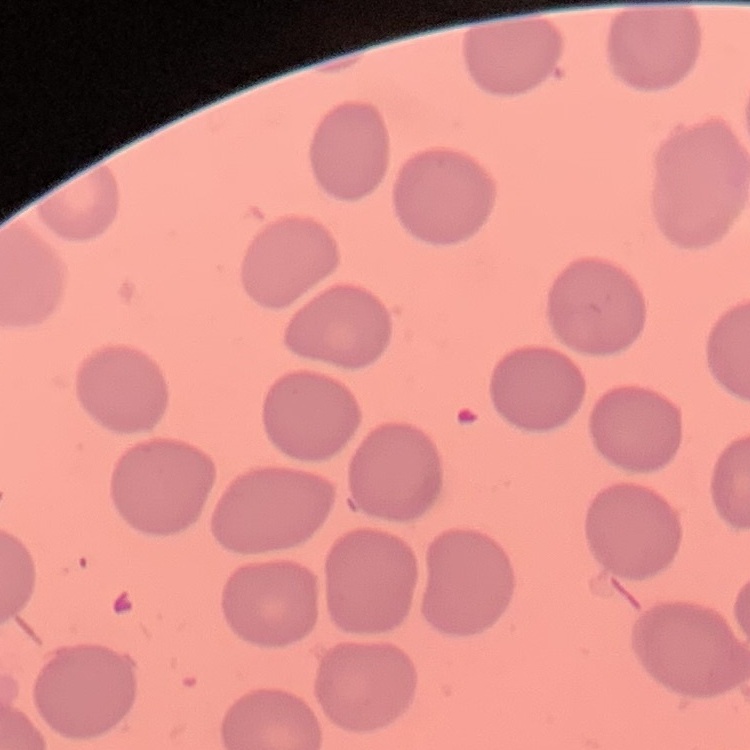
Summary:
  - Red blood cell morphology: no rouleaux formation
  - Image type: one tile cut from a larger photomicrograph
  - Stain: Field's or Giemsa
  - Preparation: thin blood film